Describe the morphology of the red blood cells.
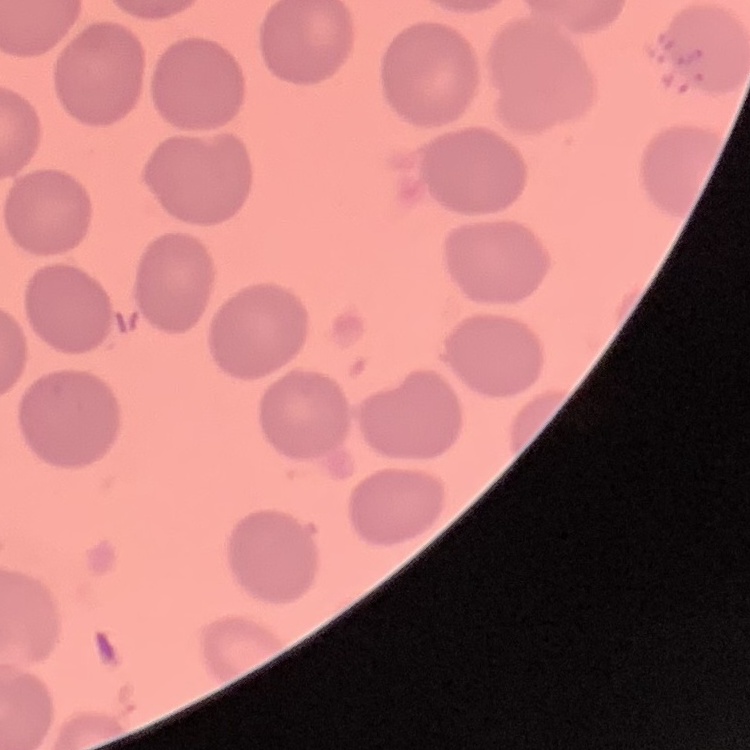

No rouleaux formation.

Stained with either Field's or Giemsa. Square crop of a larger photomicrograph. Thin blood film.